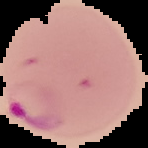

Image is 148×148 pixels. Result: malaria parasites identified. From a thin blood film. The area outside the segmented cell region is set to black.